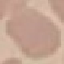

Result: negative for malaria parasites. Cell patch, automatically extracted from a larger field of view and resized to 64 × 64 pixels. Photographed with a smartphone camera at the microscope eyepiece. Giemsa stain. Thin blood smear.